Evaluate for Plasmodium parasites.
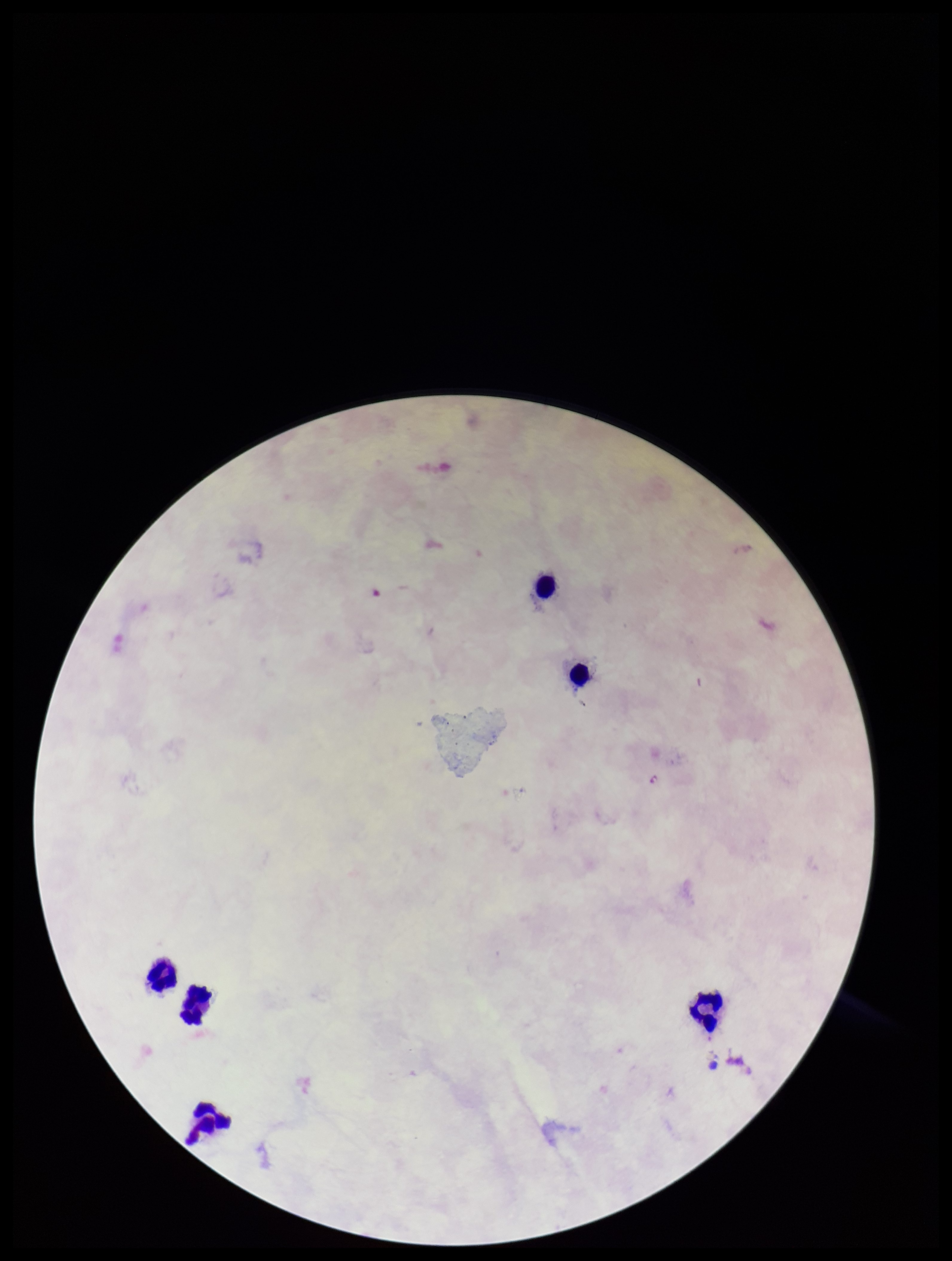
None detected.

Summary:
  - Leukocyte count: 6
  - Parasite count: 0
  - Image size: 952×1261 pixels
  - Preparation: thick smear
  - Stain: Giemsa
  - Patient malaria status: negative
  - Field of view: single
  - Capture: smartphone photograph through the microscope eyepiece